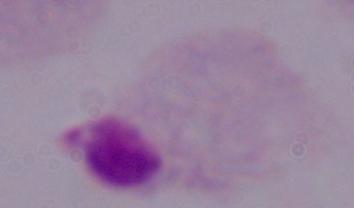
Summary:
  - Modality: photomicrograph
  - Identification: trichomonad
  - Magnification: 1000x